Comment on the morphology of the red blood cells.
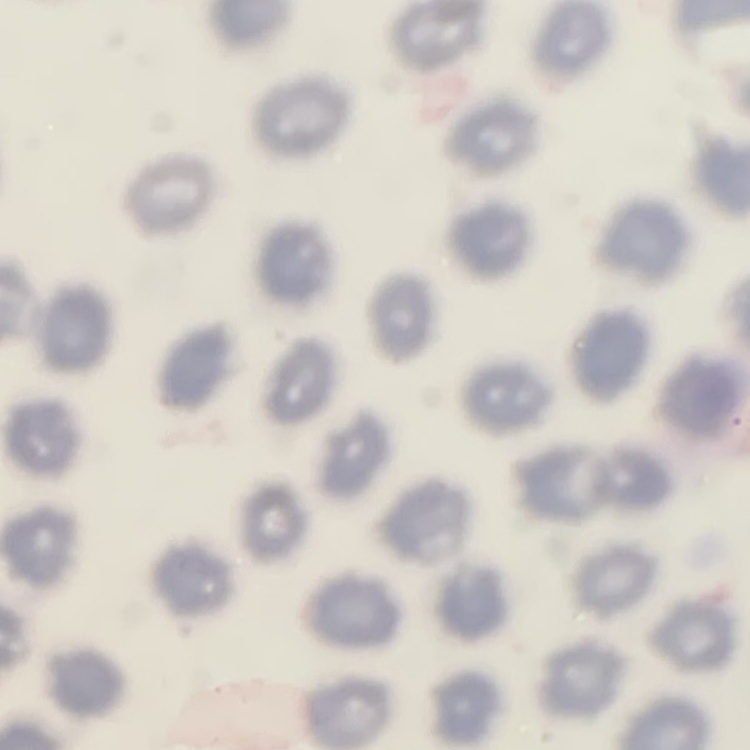

They show no rouleaux formation.

Summary:
  - Image type: square crop of a larger photomicrograph
  - Preparation: thin blood smear
  - Stain: Field's or Giemsa